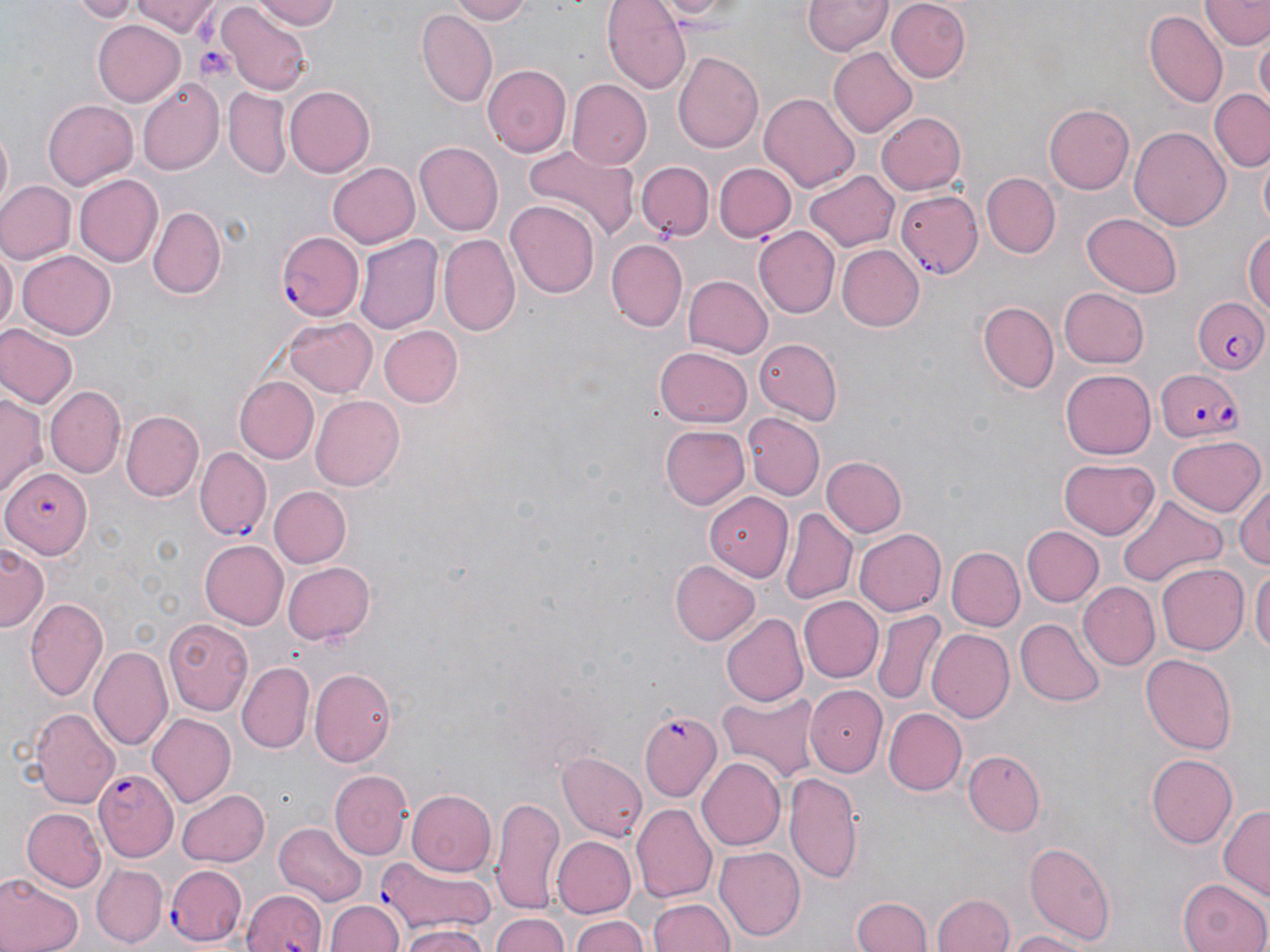

Summary:
  - Coordinate format: approximate bounding boxes as [x1, y1, x2, y2] in pixels
  - Uninfected red blood cell locations: [70, 0, 141, 21], [135, 0, 221, 37], [248, 0, 344, 29], [446, 0, 531, 24], [603, 0, 690, 93], [641, 0, 743, 22], [803, 0, 891, 57], [885, 0, 972, 82], [1203, 0, 1268, 51], [220, 4, 309, 94], [228, 7, 335, 59], [1144, 11, 1226, 109], [418, 12, 495, 107], [93, 21, 183, 105], [1255, 36, 1269, 111], [827, 48, 918, 138], [674, 51, 764, 152], [483, 64, 573, 157], [137, 78, 225, 174], [566, 80, 651, 170], [285, 87, 375, 177], [224, 89, 291, 179], [1208, 91, 1269, 172], [758, 93, 861, 192], [44, 99, 137, 189], [1044, 103, 1135, 194], [876, 111, 969, 195], [1129, 124, 1232, 229], [0, 127, 12, 215], [519, 141, 640, 240], [415, 143, 503, 235], [1257, 155, 1269, 238], [326, 161, 421, 249], [637, 161, 713, 240], [714, 162, 795, 241], [804, 168, 898, 251], [73, 172, 162, 265], [982, 172, 1060, 258], [0, 180, 75, 265], [896, 191, 984, 277], [505, 200, 599, 298], [148, 208, 224, 298], [1081, 212, 1184, 298], [755, 227, 839, 317], [1244, 228, 1270, 318], [355, 232, 442, 335], [440, 234, 521, 335], [606, 240, 687, 331], [836, 244, 923, 330], [0, 245, 17, 339], [18, 249, 117, 340], [682, 274, 773, 359], [1057, 287, 1150, 368], [976, 300, 1060, 393], [284, 317, 376, 398], [0, 324, 78, 411], [377, 325, 462, 408], [753, 336, 844, 423], [655, 346, 753, 428], [1059, 367, 1156, 457], [233, 375, 319, 463], [47, 385, 126, 478], [0, 391, 44, 496], [310, 395, 404, 490], [123, 410, 202, 499], [744, 414, 825, 501], [659, 424, 750, 510], [1166, 434, 1266, 515], [821, 455, 908, 538], [1058, 458, 1160, 538], [1233, 479, 1270, 572], [268, 486, 350, 567], [1116, 492, 1224, 588], [706, 493, 794, 578], [780, 507, 857, 604], [1022, 526, 1103, 606], [855, 528, 945, 616], [199, 540, 288, 630], [0, 543, 50, 628], [949, 546, 1023, 630], [281, 560, 376, 645], [671, 561, 761, 646], [1156, 563, 1249, 655], [1251, 565, 1269, 666], [1077, 582, 1159, 671], [25, 596, 107, 699], [799, 596, 882, 682], [873, 611, 944, 705], [723, 615, 809, 706], [163, 617, 252, 713], [1014, 618, 1106, 708], [930, 628, 1014, 722], [91, 646, 174, 749], [1141, 651, 1238, 754], [238, 662, 314, 752], [309, 668, 397, 768], [805, 684, 889, 776], [715, 688, 824, 783], [29, 708, 119, 809], [884, 709, 967, 796], [146, 713, 236, 807], [558, 749, 648, 841], [962, 751, 1046, 835], [1149, 752, 1238, 847], [696, 758, 785, 851], [331, 769, 411, 859], [784, 771, 863, 884], [175, 788, 272, 868], [408, 788, 498, 874], [491, 793, 566, 914], [632, 804, 717, 904], [1218, 804, 1270, 903], [23, 808, 106, 891], [275, 822, 367, 907], [551, 835, 638, 918], [1024, 840, 1117, 945], [715, 846, 807, 941], [93, 864, 167, 946], [0, 876, 80, 952], [1178, 877, 1270, 952], [244, 890, 327, 952], [932, 891, 1015, 952], [852, 895, 932, 952], [648, 897, 734, 952], [327, 901, 403, 952], [489, 912, 573, 952], [569, 913, 652, 952], [398, 925, 490, 952], [1006, 930, 1090, 951]
  - Plasmodium falciparum-infected red blood cell locations: [278, 231, 364, 320], [1190, 295, 1270, 375], [1155, 365, 1244, 439], [194, 446, 270, 538], [2, 465, 95, 556], [641, 711, 722, 800], [94, 769, 177, 863], [377, 862, 494, 939], [165, 864, 249, 945]
  - Platelet locations: [196, 42, 234, 81]
  - Slide-level diagnosis: Plasmodium falciparum
  - Magnification: 1000x
  - Field of view: one of a larger specimen
  - Modality: optical microscopy
  - Image size: 1270×952 pixels
  - Stain: May-Grünwald-Giemsa
  - Preparation: thin blood film